Classify this cell by malaria status.
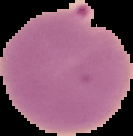
Parasitized.

Cell region segmented out of the field of view; the surrounding area is masked to black. Image is 133×136 pixels. From a thin blood smear.